Name the cell type shown.
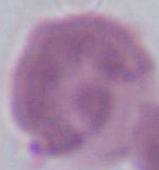
An erythrocyte.

Summary:
  - Modality: photomicrograph
  - Magnification: 1000x